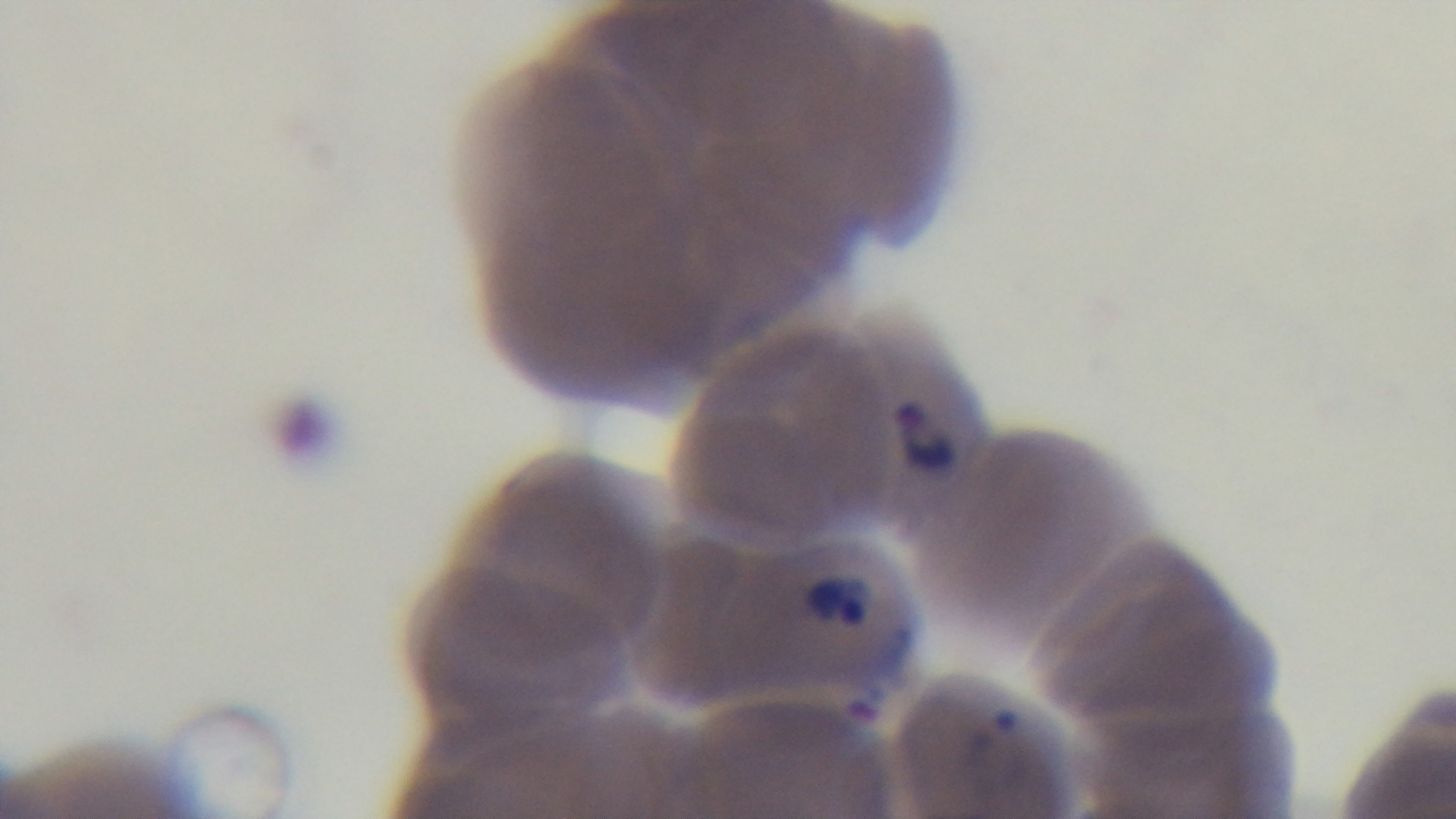

preparation = thin smear
field of view = single
modality = light microscopy
malaria status = positive
objective = 100x oil immersion
capture = mounted 4K digital camera
stain = Giemsa